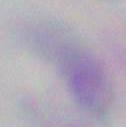
{
  "modality": "photomicrograph",
  "identification": "Toxoplasma gondii",
  "magnification": "1000x"
}